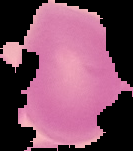

Malaria status: uninfected. Image is 133×151 pixels. Segmented cell region on a black background. From a thin blood smear.